Assess this cell for malaria.
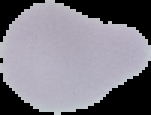

It is uninfected.

{
  "preparation": "thin blood film",
  "image_size": "151×115 pixels",
  "image_type": "segmented cell region on a black background"
}